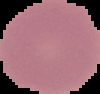

image_size: 100×94 pixels
malaria_status: uninfected
image_type: cell region segmented out of the field of view; surrounding area masked to black
preparation: thin blood smear